Name the parasite shown.
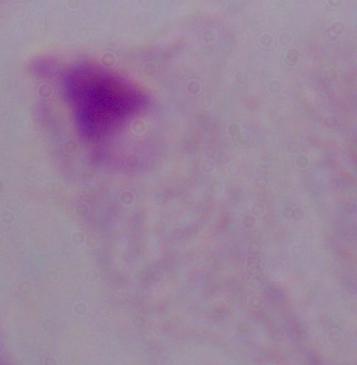
A trichomonad.

Summary:
  - Magnification: 1000x
  - Modality: micrograph